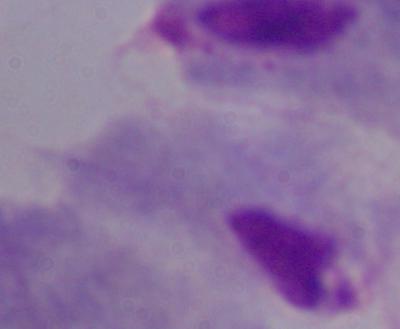
{
  "magnification": "1000x",
  "modality": "micrograph",
  "identification": "trichomonad"
}